Assess the morphology of the erythrocytes.
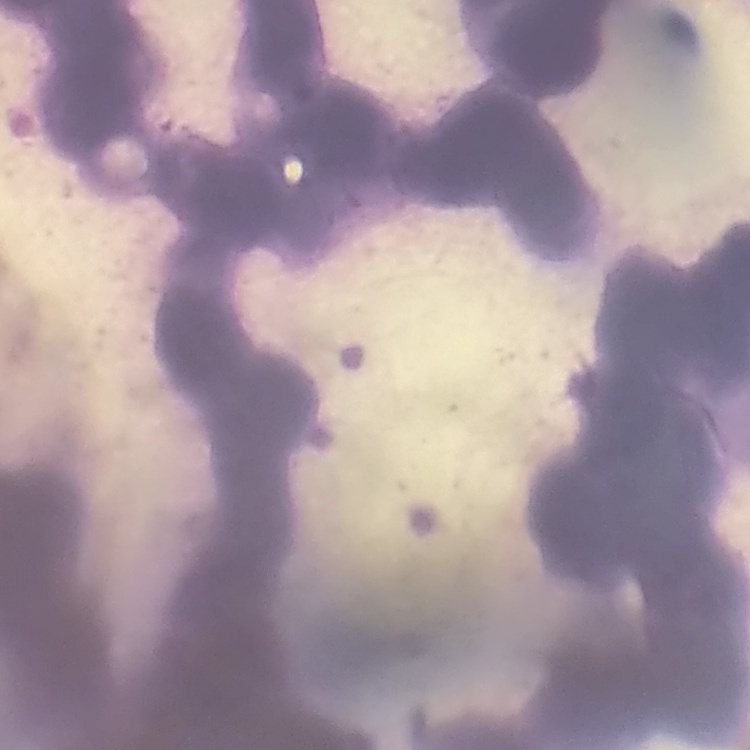

They show rouleaux formation.

image_type: one tile cut from a larger photomicrograph
preparation: thin peripheral smear
stain: Field's or Giemsa